Assess this cell for malaria.
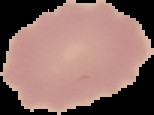
It is uninfected.

Summary:
  - Preparation: thin blood film
  - Image type: cell region segmented out of the field of view; surrounding area masked to black
  - Image size: 154×115 pixels